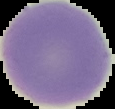
preparation = thin blood smear
image type = segmented cell region on a black background
malaria status = uninfected
image size = 115×109 pixels